Identify the parasite.
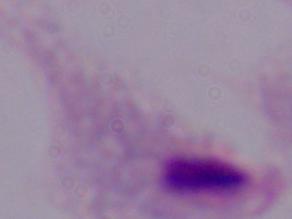
A trichomonad.

magnification: 1000x
modality: micrograph